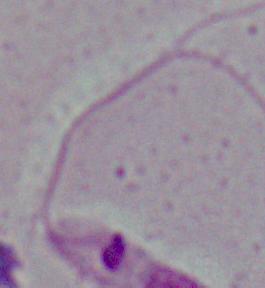
Summary:
  - Identification: Leishmania
  - Magnification: 1000x
  - Modality: photomicrograph